State the blood parasite species.
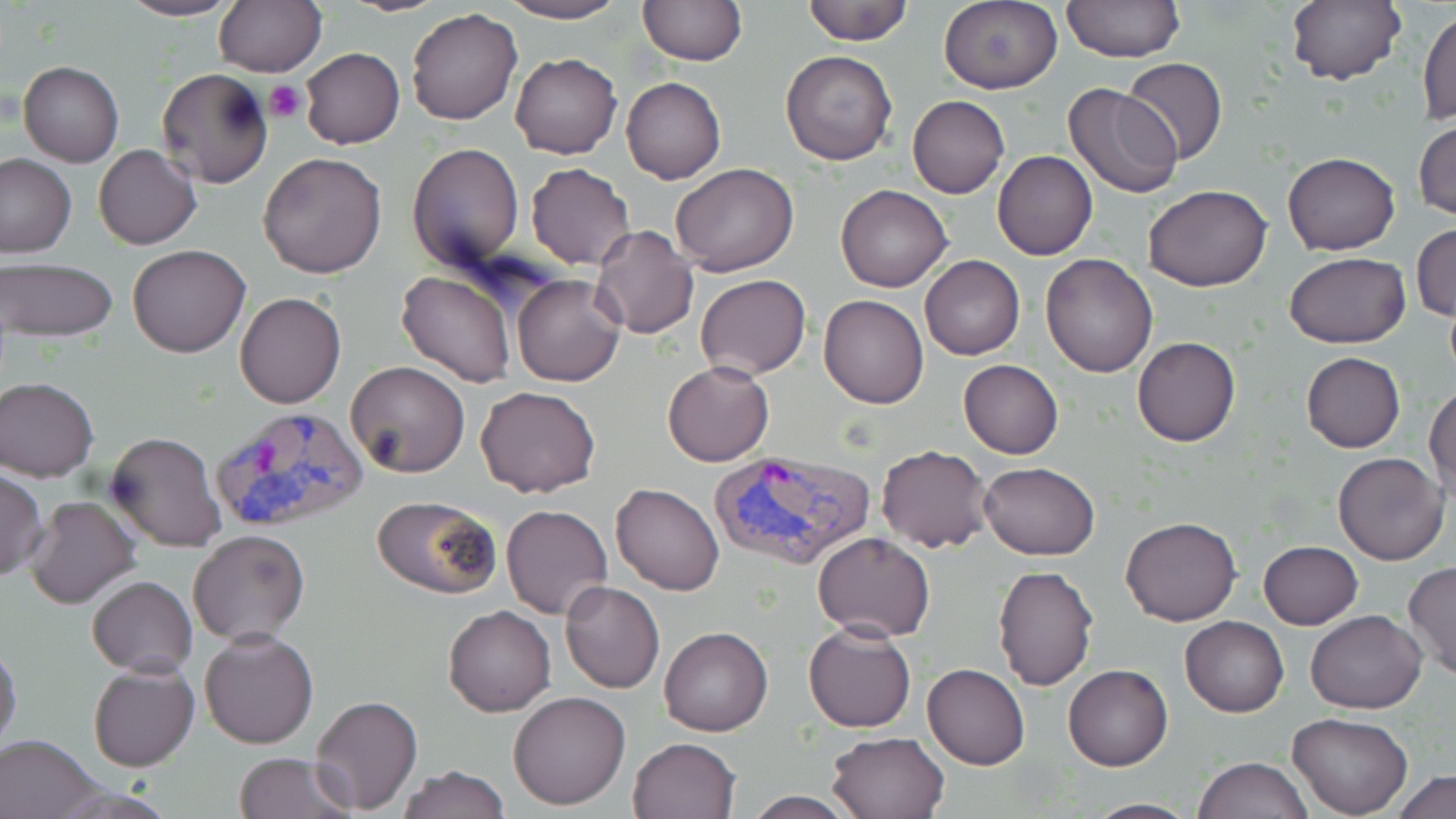

Plasmodium vivax.

Approximate bounding boxes as named x1/y1/x2/y2 corners in pixels. Platelet locations: (x1=266, y1=80, x2=306, y2=123). Uninfected red blood cell locations: (x1=117, y1=0, x2=242, y2=22), (x1=213, y1=0, x2=325, y2=77), (x1=336, y1=0, x2=453, y2=17), (x1=497, y1=0, x2=629, y2=23), (x1=801, y1=0, x2=914, y2=45), (x1=1062, y1=0, x2=1184, y2=64), (x1=1285, y1=0, x2=1406, y2=87), (x1=638, y1=1, x2=747, y2=66), (x1=939, y1=1, x2=1063, y2=93), (x1=1418, y1=7, x2=1455, y2=124), (x1=407, y1=8, x2=524, y2=126), (x1=299, y1=47, x2=404, y2=149), (x1=781, y1=49, x2=897, y2=166), (x1=510, y1=52, x2=621, y2=159), (x1=1120, y1=57, x2=1229, y2=165), (x1=18, y1=61, x2=124, y2=166), (x1=155, y1=68, x2=274, y2=190), (x1=621, y1=76, x2=726, y2=185), (x1=1061, y1=83, x2=1184, y2=200), (x1=907, y1=95, x2=1009, y2=198), (x1=1414, y1=117, x2=1455, y2=221), (x1=406, y1=141, x2=525, y2=272), (x1=95, y1=144, x2=201, y2=249), (x1=992, y1=150, x2=1098, y2=261), (x1=1282, y1=151, x2=1400, y2=255), (x1=256, y1=152, x2=388, y2=279), (x1=0, y1=154, x2=75, y2=258), (x1=526, y1=163, x2=636, y2=270), (x1=670, y1=163, x2=799, y2=278), (x1=1143, y1=183, x2=1272, y2=292), (x1=836, y1=185, x2=953, y2=293), (x1=1412, y1=222, x2=1455, y2=323), (x1=590, y1=224, x2=700, y2=339), (x1=127, y1=243, x2=251, y2=357), (x1=1285, y1=252, x2=1409, y2=347), (x1=919, y1=254, x2=1025, y2=360), (x1=1041, y1=254, x2=1156, y2=376), (x1=1, y1=259, x2=118, y2=343), (x1=396, y1=271, x2=519, y2=388), (x1=512, y1=274, x2=626, y2=387), (x1=695, y1=274, x2=811, y2=380), (x1=235, y1=291, x2=346, y2=409), (x1=819, y1=293, x2=929, y2=409), (x1=1132, y1=336, x2=1240, y2=447), (x1=1301, y1=352, x2=1405, y2=453), (x1=958, y1=359, x2=1063, y2=459), (x1=345, y1=360, x2=471, y2=478), (x1=662, y1=360, x2=775, y2=467), (x1=1, y1=376, x2=99, y2=480), (x1=1427, y1=384, x2=1456, y2=499), (x1=475, y1=385, x2=601, y2=498), (x1=105, y1=430, x2=227, y2=553), (x1=875, y1=444, x2=994, y2=553), (x1=1333, y1=452, x2=1449, y2=565), (x1=978, y1=462, x2=1101, y2=560), (x1=0, y1=468, x2=47, y2=581), (x1=610, y1=483, x2=724, y2=596), (x1=24, y1=495, x2=141, y2=608), (x1=371, y1=495, x2=501, y2=598), (x1=499, y1=504, x2=612, y2=620), (x1=1119, y1=515, x2=1241, y2=626), (x1=187, y1=528, x2=311, y2=645), (x1=813, y1=531, x2=935, y2=643), (x1=1258, y1=541, x2=1364, y2=630), (x1=1404, y1=561, x2=1456, y2=681), (x1=992, y1=564, x2=1098, y2=691), (x1=86, y1=575, x2=197, y2=676), (x1=559, y1=579, x2=666, y2=693), (x1=443, y1=604, x2=556, y2=718), (x1=1305, y1=610, x2=1427, y2=714), (x1=1180, y1=615, x2=1289, y2=717), (x1=803, y1=622, x2=916, y2=733), (x1=658, y1=626, x2=773, y2=737), (x1=200, y1=628, x2=319, y2=750), (x1=0, y1=643, x2=23, y2=755), (x1=923, y1=662, x2=1031, y2=770), (x1=89, y1=663, x2=199, y2=772), (x1=1062, y1=663, x2=1173, y2=771), (x1=507, y1=691, x2=632, y2=811), (x1=309, y1=694, x2=424, y2=816), (x1=1289, y1=712, x2=1413, y2=818), (x1=825, y1=730, x2=949, y2=819), (x1=0, y1=733, x2=102, y2=819), (x1=627, y1=736, x2=741, y2=819), (x1=232, y1=752, x2=359, y2=819), (x1=1193, y1=756, x2=1311, y2=819), (x1=395, y1=764, x2=511, y2=819), (x1=1391, y1=770, x2=1456, y2=819), (x1=739, y1=792, x2=860, y2=818), (x1=1082, y1=798, x2=1201, y2=817). Plasmodium vivax-infected red blood cell locations: (x1=209, y1=404, x2=371, y2=536), (x1=707, y1=447, x2=876, y2=572). May-Grünwald-Giemsa stain. Captured at 1000x magnification. Optical microscopy. Thin blood film. One field of a larger specimen. Image is 1456×819 pixels.